Identify the preparation type.
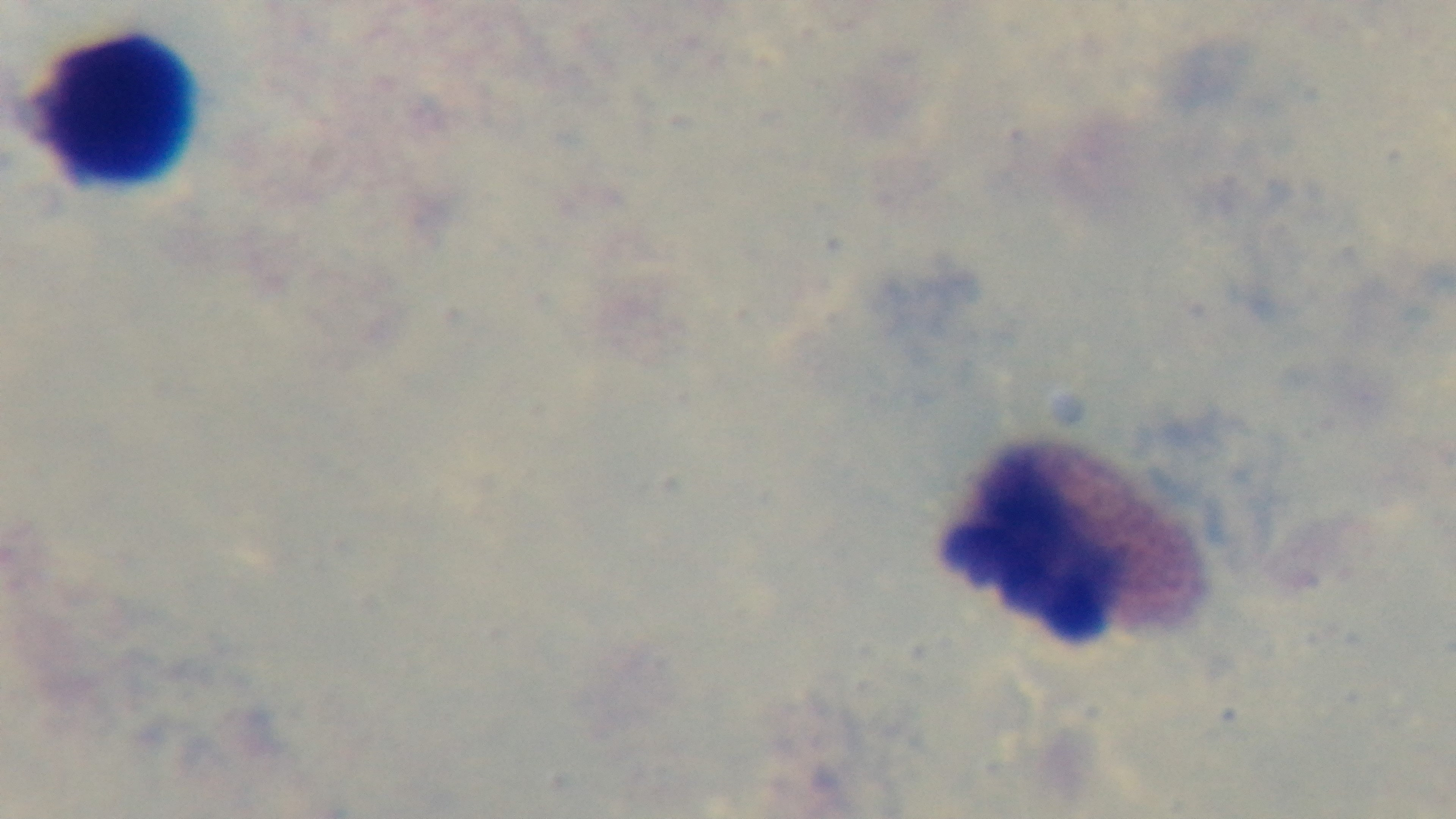

It is a thick blood film.

One field from the slide. Mounted 4K digital camera. 100x oil-immersion objective. Light microscopy. Malaria status: negative. Giemsa stain.